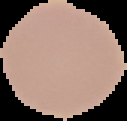
Summary:
  - Result: no malaria parasites seen
  - Preparation: thin blood smear
  - Image type: segmented cell region on a black background
  - Image size: 127×121 pixels